Assess this cell for malaria.
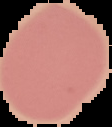

It is uninfected.

image type = cell region segmented out of the field of view; surrounding area masked to black
preparation = thin blood film
image size = 112×127 pixels